Identify the cell.
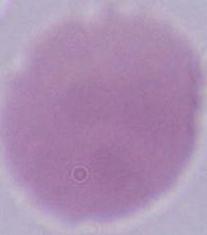

An erythrocyte.

Summary:
  - Modality: photomicrograph
  - Magnification: 1000x